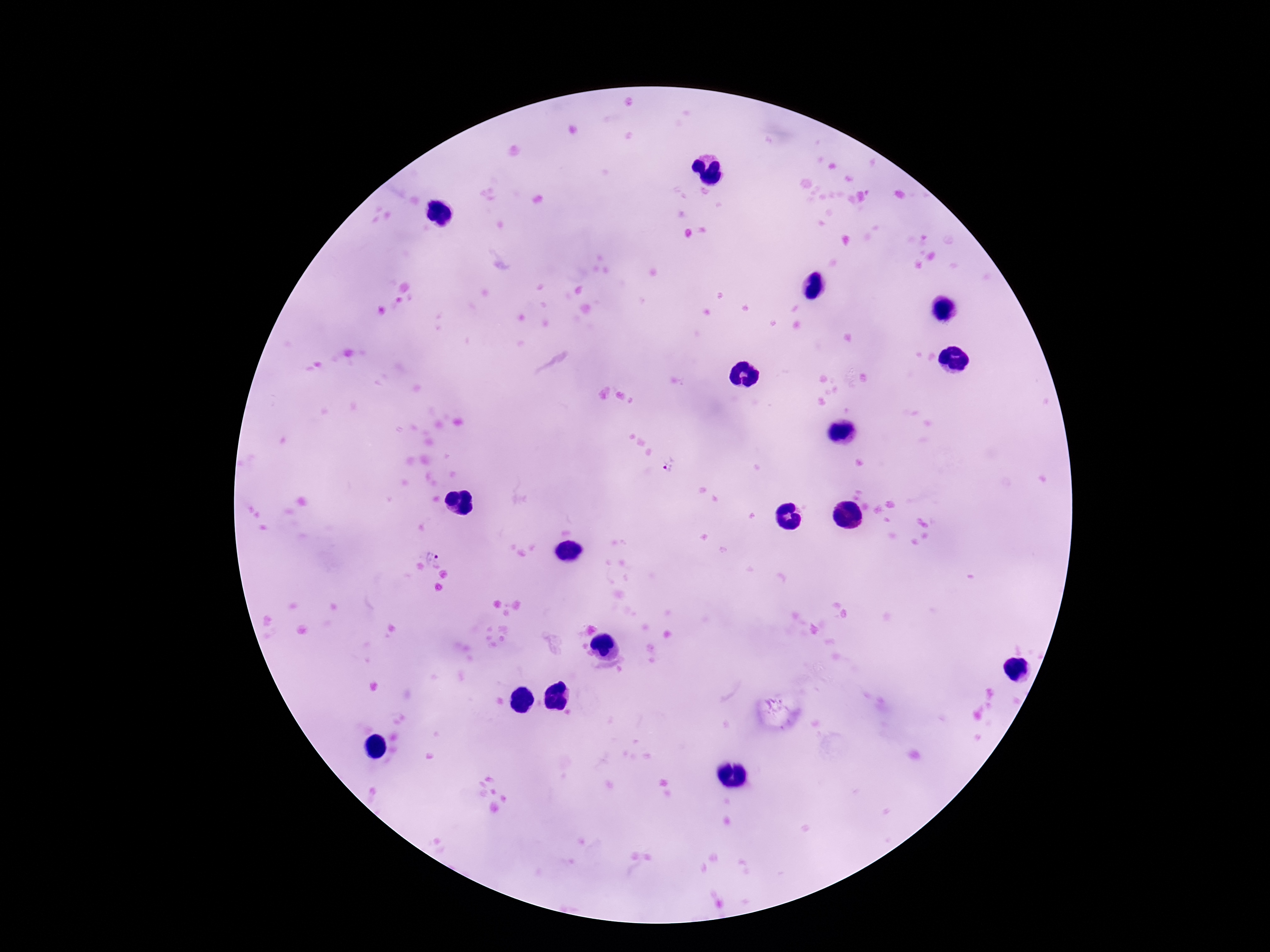
Approximate centers as [x, y] in pixels. Plasmodium parasite locations: [669, 465], [436, 558]. Single field of view. Giemsa stain. Patient malaria status: infected. Thick blood film. Image is 1270×952 pixels. Smartphone photograph taken through the microscope eyepiece. 100x magnification.